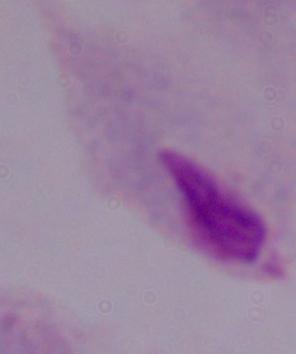
Summary:
  - Identification: trichomonad
  - Modality: photomicrograph
  - Magnification: 1000x